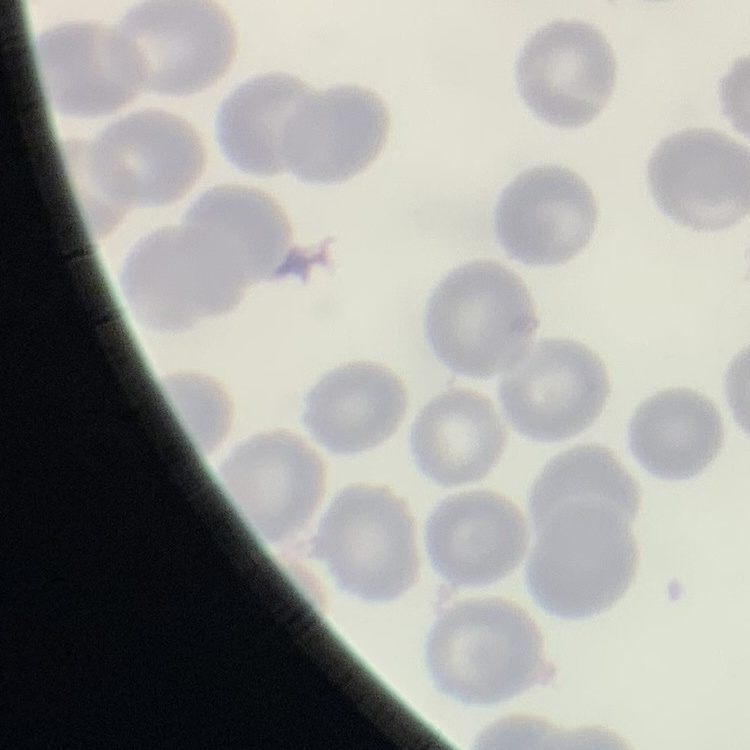

Summary:
  - Erythrocyte morphology: no rouleaux formation
  - Stain: Field's or Giemsa
  - Image type: one tile cut from a larger photomicrograph
  - Preparation: thin blood smear